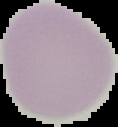
Malaria status: uninfected. Image is 118×127 pixels. Cell region segmented out of the field of view; the surrounding area is masked to black. From a thin blood smear.